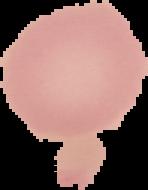 Segmented cell region on a black background. Result: negative for Plasmodium parasites. Image is 148×190 pixels. From a thin blood smear.